State which parasite is depicted.
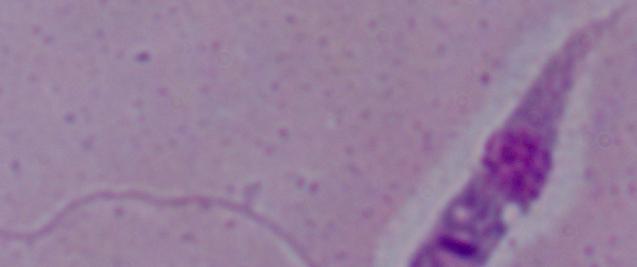

Leishmania.

Summary:
  - Modality: photomicrograph
  - Magnification: 1000x